Locate every blood parasite and identify its species.
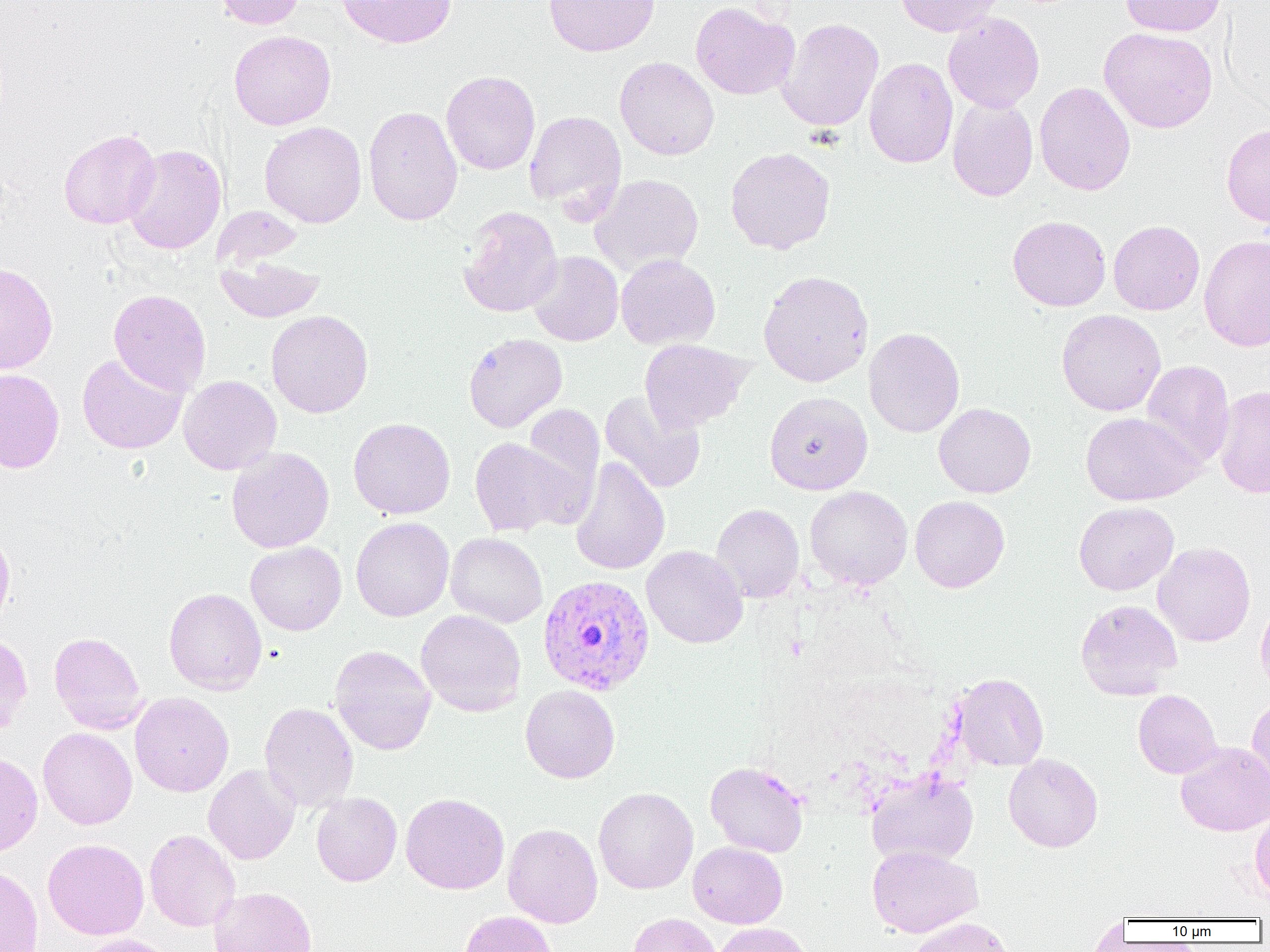
Approximate bounding boxes as (x1,y1)-(x2,y2) corner pairs in pixels.
Plasmodium vivax-infected red blood cells: (537,574)-(655,696).
No Plasmodium falciparum, Plasmodium ovale, Plasmodium malariae, Babesia divergens, or Trypanosoma brucei observed.

Summary:
  - Uninfected red blood cell locations: (214,0)-(307,30), (336,0)-(457,48), (544,0)-(659,57), (895,0)-(1004,36), (1120,0)-(1225,36), (690,1)-(798,100), (943,12)-(1045,113), (777,18)-(884,132), (1099,27)-(1218,133), (229,30)-(336,130), (614,56)-(719,161), (864,57)-(958,168), (441,70)-(540,175), (1034,81)-(1136,196), (948,97)-(1038,201), (362,105)-(463,226), (524,110)-(627,218), (259,121)-(367,228), (1221,123)-(1270,228), (58,128)-(161,229), (123,144)-(227,254), (725,146)-(836,255), (589,174)-(704,277), (458,206)-(563,317), (1007,215)-(1111,311), (1108,220)-(1205,315), (1199,235)-(1270,352), (527,251)-(624,346), (216,254)-(324,322), (616,254)-(720,350), (0,263)-(58,374), (758,269)-(874,387), (108,289)-(211,395), (1056,309)-(1166,416), (266,310)-(374,418), (863,327)-(965,437), (463,333)-(567,432), (639,339)-(752,432), (77,352)-(188,454), (1140,360)-(1235,469), (0,368)-(65,473), (178,375)-(282,475), (1214,385)-(1270,498), (600,390)-(706,494), (764,392)-(872,495), (933,402)-(1036,498), (522,403)-(605,503), (1080,411)-(1202,505), (348,417)-(455,519), (469,437)-(582,538), (226,447)-(334,553), (570,457)-(670,575), (805,486)-(913,589), (910,495)-(1010,593), (1074,501)-(1179,595), (711,503)-(804,602), (351,517)-(454,622), (0,526)-(15,629), (445,532)-(548,627), (245,541)-(346,635), (1153,542)-(1256,647), (641,545)-(748,648), (164,587)-(267,695), (1255,597)-(1270,699), (1075,599)-(1182,700), (416,609)-(526,716), (49,631)-(146,734), (0,632)-(33,737), (330,644)-(436,755), (951,673)-(1049,771), (520,684)-(620,783), (1133,689)-(1222,778), (130,692)-(234,797), (1247,697)-(1270,796), (259,702)-(358,812), (38,728)-(137,829), (1175,741)-(1270,836), (0,752)-(43,856), (1004,753)-(1103,852), (705,761)-(809,857), (203,764)-(300,865), (866,771)-(978,867), (593,787)-(698,894), (311,792)-(402,886), (401,793)-(509,894), (1249,807)-(1270,904), (503,823)-(603,927), (144,829)-(240,931), (43,838)-(149,939), (688,841)-(787,928), (867,845)-(983,937), (0,865)-(43,952), (209,886)-(317,952), (460,911)-(558,952), (628,912)-(722,952), (1087,915)-(1130,951), (908,916)-(1015,952), (712,922)-(812,952), (76,933)-(176,952)
  - Slide-level diagnosis: Plasmodium vivax
  - Magnification: 1000x
  - Preparation: thin blood smear
  - Field of view: one of a larger specimen
  - Image size: 1270×952 pixels
  - Modality: light microscopy